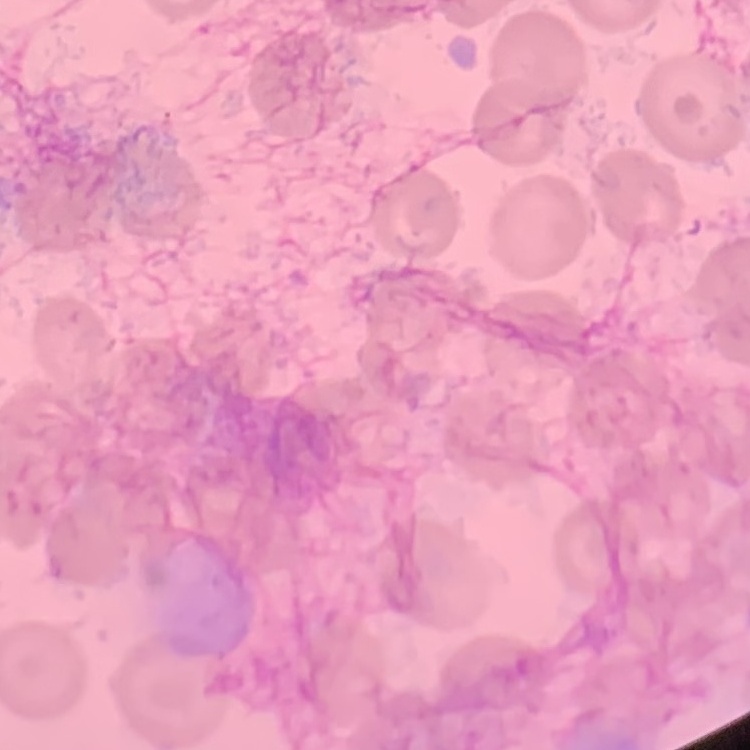
erythrocyte morphology = no rouleaux formation
preparation = thin blood film
image type = square crop of a larger photomicrograph
stain = Field's or Giemsa